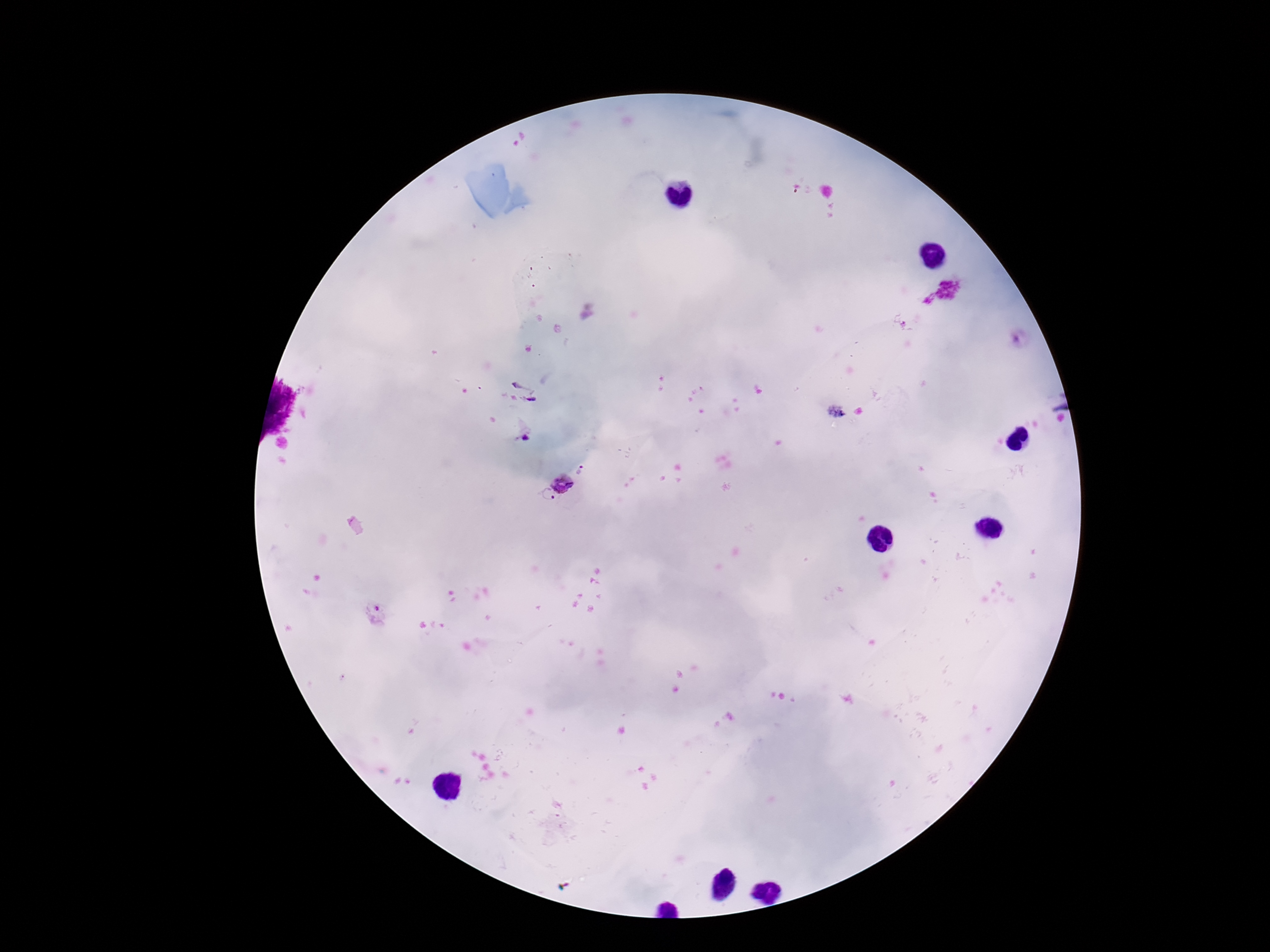
Approximate object centers, in pixels from the top-left corner. Plasmodium parasite locations: (x=949, y=288), (x=930, y=301), (x=525, y=389), (x=525, y=436), (x=563, y=484), (x=547, y=496), (x=376, y=614). Patient malaria status: positive. Image is 1270×952 pixels. Giemsa stain. Single field of view. Photographed through the microscope eyepiece with a smartphone camera. 100x magnification. Thick blood film.